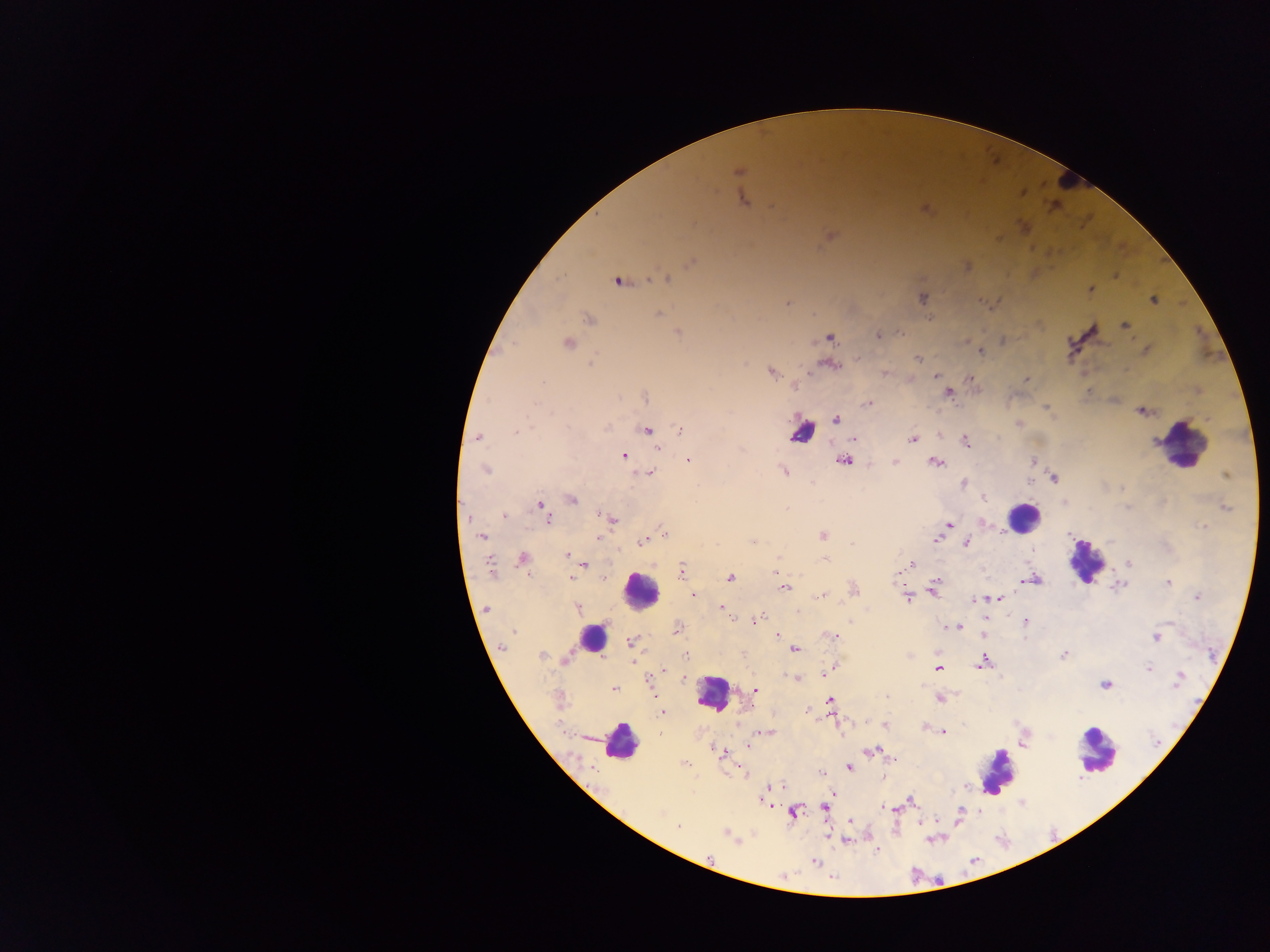
preparation: thick blood film
image_size: 1270×952 pixels
country: Ghana
leukocyte_locations: 'approximate centers as {x, y} in pixels: {1063, 180}, {802, 433}, {1180, 445}, {1023, 517}, {1085, 561}, {641, 590}, {592, 638}, {713, 694}, {620, 742}, {1096, 752}, {997, 770}'
capture: mobile-phone photograph through a microscope
field_of_view: single
plasmodium_parasite_locations: 'approximate centers as {x, y} in pixels: {739, 172}, {742, 199}, {774, 208}, {830, 235}, {692, 262}, {967, 266}, {667, 278}, {617, 281}, {1091, 290}, {922, 298}, {980, 300}, {1153, 301}, {787, 303}, {659, 315}, {589, 319}, {1125, 325}, {678, 333}, {901, 333}, {878, 335}, {830, 337}, {1003, 341}, {567, 342}, {981, 352}, {918, 358}, {591, 364}, {833, 366}, {771, 372}, {884, 373}, {935, 376}, {969, 379}, {1026, 380}, {795, 387}, {949, 393}, {646, 397}, {868, 403}, {1046, 408}, {1141, 411}, {836, 419}, {1020, 423}, {606, 428}, {647, 430}, {681, 430}, {516, 433}, {478, 437}, {854, 438}, {912, 439}, {966, 441}, {656, 448}, {623, 455}, {688, 460}, {843, 461}, {895, 462}, {935, 462}, {1034, 462}, {485, 470}, {784, 471}, {649, 473}, {1226, 475}, {1053, 478}, {962, 483}, {983, 498}, {572, 499}, {541, 505}, {1226, 508}, {599, 514}, {504, 515}, {605, 515}, {548, 519}, {612, 519}, {982, 522}, {949, 525}, {1202, 526}, {664, 532}, {822, 535}, {482, 537}, {597, 539}, {936, 540}, {644, 541}, {754, 541}, {967, 543}, {852, 544}, {566, 555}, {522, 559}, {778, 559}, {825, 559}, {1129, 563}, {584, 565}, {911, 565}, {490, 566}, {682, 571}, {571, 578}, {604, 578}, {731, 578}, {1034, 580}, {1168, 582}, {936, 583}, {934, 587}, {784, 588}, {854, 590}, {693, 595}, {822, 596}, {906, 597}, {1197, 597}, {997, 598}, {975, 600}, {721, 606}, {577, 608}, {487, 609}, {796, 611}, {732, 619}, {756, 621}, {1025, 621}, {957, 627}, {678, 629}, {514, 632}, {777, 635}, {833, 636}, {1156, 637}, {631, 642}, {502, 647}, {794, 649}, {686, 655}, {1063, 655}, {542, 656}, {566, 658}, {983, 662}, {1148, 668}, {938, 669}, {663, 671}, {827, 672}, {796, 678}, {1179, 678}, {684, 680}, {1105, 684}, {613, 689}, {755, 691}, {887, 697}, {939, 699}, {559, 700}, {830, 700}, {808, 711}, {662, 712}, {868, 722}, {885, 725}, {926, 728}, {768, 732}, {943, 732}, {748, 746}, {872, 751}, {721, 753}, {892, 759}, {685, 764}, {849, 767}, {821, 773}, {766, 789}, {911, 800}, {825, 807}, {887, 809}, {793, 813}, {677, 826}, {727, 834}, {845, 840}, {815, 862}'